Classify this cell by malaria status.
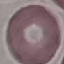

Uninfected.

Acquired by smartphone through the microscope eyepiece. Cell patch, automatically extracted from a larger field of view and resized to 64 × 64 pixels. Thin blood smear. Giemsa-stained preparation.